Assess this cell for malaria.
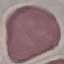

Uninfected.

Acquired by smartphone through the microscope eyepiece. Automatically extracted cell patch, resized to 64 × 64 pixels. Thin smear of blood. Giemsa-stained preparation.